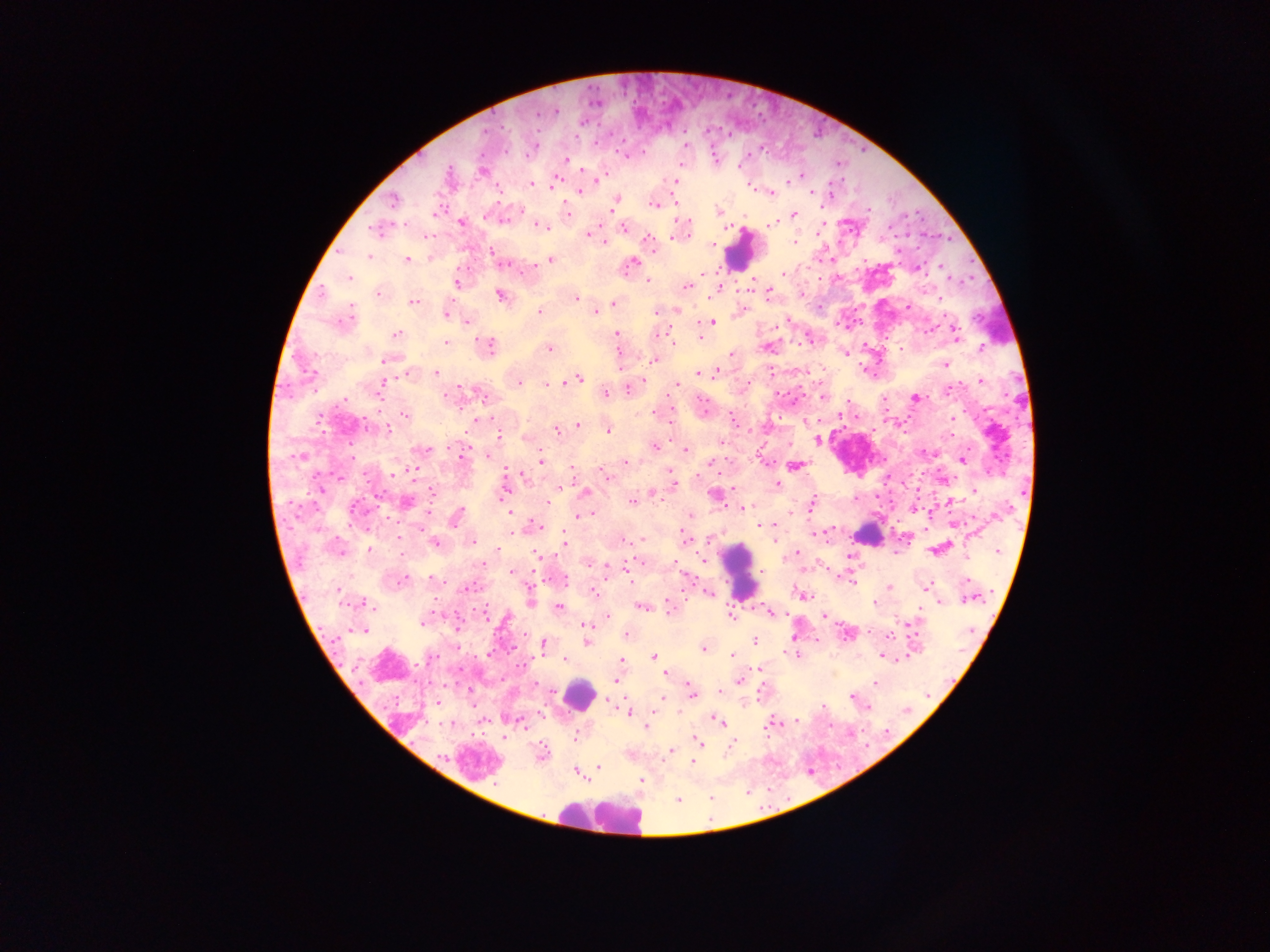

country = Ghana
leukocyte locations = approximate centers as x y in pixels: 740 250; 866 534; 739 571; 579 693; 602 817
malaria parasite locations = approximate centers as x y in pixels: 555 112; 486 131; 684 146; 532 148; 625 155; 565 161; 679 162; 482 171; 794 176; 676 178; 596 180; 553 183; 530 184; 751 188; 578 191; 812 191; 772 192; 394 199; 614 202; 654 204; 868 209; 718 211; 566 212; 793 215; 503 220; 461 222; 772 222; 540 225; 623 227; 376 229; 681 230; 589 234; 678 234; 793 241; 603 242; 650 242; 711 244; 490 251; 368 256; 429 257; 407 259; 552 259; 632 261; 506 264; 941 266; 531 267; 918 268; 701 273; 782 273; 349 278; 646 280; 455 283; 686 285; 751 288; 718 289; 768 292; 378 294; 500 295; 575 297; 414 302; 614 303; 908 306; 676 310; 594 311; 656 311; 540 312; 446 313; 343 319; 466 322; 711 322; 955 333; 396 334; 616 335; 700 336; 446 343; 672 343; 486 347; 549 348; 900 348; 981 348; 731 353; 844 353; 618 354; 388 360; 653 360; 944 364; 715 371; 435 372; 410 373; 772 373; 698 374; 576 379; 980 380; 517 382; 567 382; 546 384; 677 384; 746 384; 381 386; 627 387; 605 392; 823 396; 915 397; 793 400; 884 400; 405 414; 951 418; 476 421; 578 425; 669 425; 386 428; 556 429; 607 430; 950 434; 497 435; 816 438; 721 442; 452 446; 654 447; 424 450; 685 450; 489 455; 301 456; 962 459; 540 460; 624 462; 795 465; 573 469; 395 471; 669 471; 604 476; 942 477; 777 485; 673 486; 319 487; 559 487; 974 490; 431 491; 504 492; 585 493; 651 493; 716 495; 854 498; 631 501; 950 501; 405 502; 546 503; 811 503; 742 507; 354 508; 913 508; 509 511; 791 511; 589 513; 582 515; 688 516; 455 517; 576 518; 758 525; 539 526; 422 528; 625 538; 642 539; 685 540; 775 540; 472 541; 564 541; 435 543; 936 548; 337 550; 368 550; 996 550; 497 551; 796 552; 538 557; 702 560; 589 564; 607 566; 626 566; 513 572; 400 578; 432 578; 852 581; 926 586; 467 587; 889 587; 593 592; 707 592; 802 595; 969 597; 530 601; 939 601; 366 603; 875 603; 642 606; 558 608; 668 608; 770 612; 731 614; 824 616; 606 617; 423 621; 913 622; 585 624; 457 627; 362 629; 625 635; 755 640; 586 642; 541 645; 702 648; 795 654; 883 654; 731 655; 653 656; 430 657; 566 658; 621 661; 758 669; 665 672; 616 679; 739 680; 875 683; 718 692; 690 693; 662 696; 851 696; 659 700; 439 701; 610 701; 868 708; 628 712; 712 718; 718 720; 796 720; 772 723; 521 724; 646 726; 505 736; 574 738; 697 741; 733 743; 671 750; 541 753; 692 762; 598 766; 579 773; 641 780; 678 798
image size = 1270×952 pixels
field of view = single
preparation = thick blood smear
capture = mobile-phone photograph through a microscope